State which cell type is depicted.
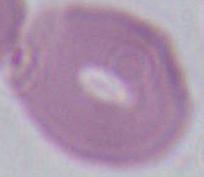

An erythrocyte.

Summary:
  - Modality: photomicrograph
  - Magnification: 1000x